Classify this cell by malaria status.
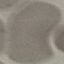

It is uninfected.

Summary:
  - Image type: automatically extracted cell patch, resized to 64 × 64 pixels
  - Capture: smartphone camera at the microscope eyepiece
  - Preparation: thin blood smear
  - Stain: Giemsa